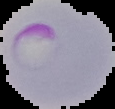
The area outside the segmented cell region is set to black. From a thin blood smear. Result: Plasmodium parasites detected. Image is 115×109 pixels.